Point out each Plasmodium parasite.
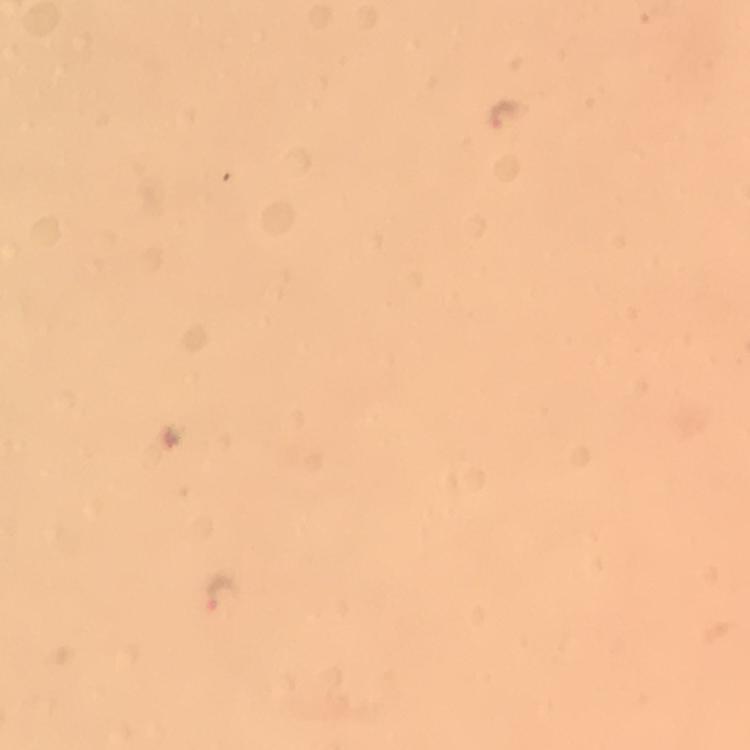
Approximate centers as {x, y} in pixels.
Plasmodium parasites: {504, 114}, {218, 593}.

image size = 750×750 pixels
stain = Giemsa
magnification = 100x
immersion oil = applied
context = from a malaria diagnostic workup
preparation = thick blood smear
cropped from = one field of view
capture = smartphone camera through the microscope